Describe the morphology of the red blood cells.
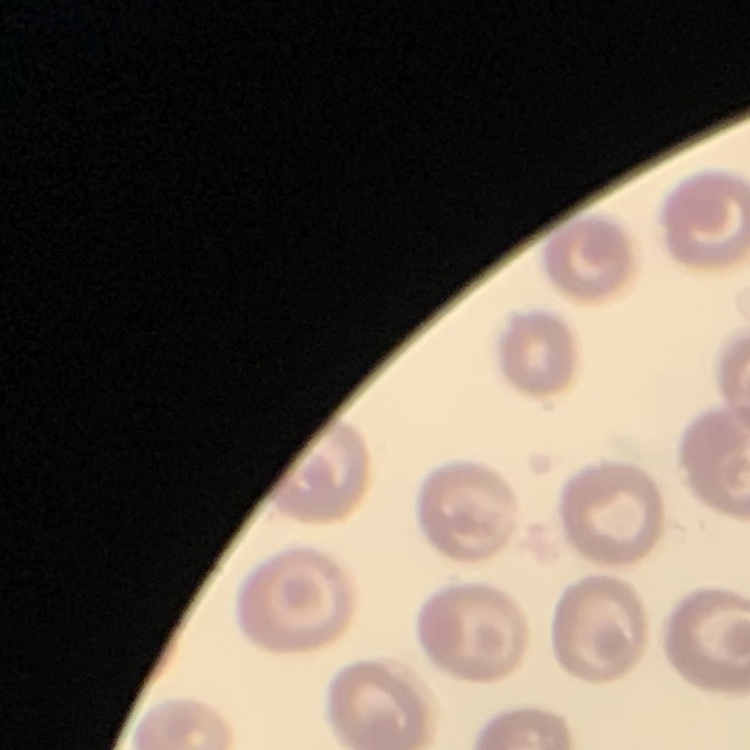
No rouleaux formation.

Square crop of a larger photomicrograph. Stained with either Field's or Giemsa. Thin blood smear.